State the blood parasite species.
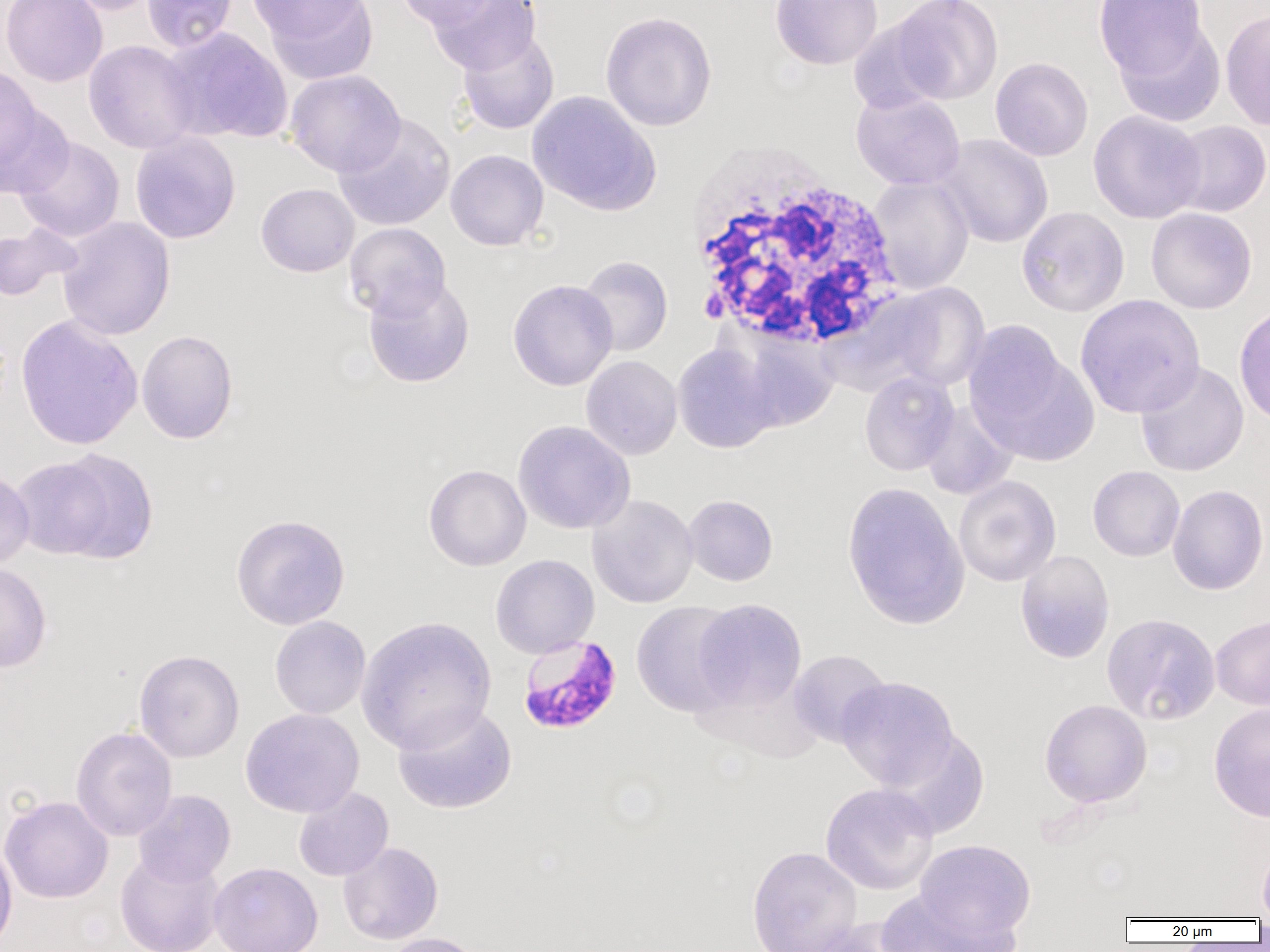

Plasmodium falciparum.

Approximate bounding boxes as [x1, y1, x2, y2] in pixels. White blood cell locations: [685, 141, 907, 355]. Uninfected red blood cell locations: [1, 0, 108, 87], [63, 0, 164, 15], [142, 0, 237, 52], [245, 0, 369, 44], [394, 0, 502, 29], [425, 0, 540, 74], [770, 0, 883, 70], [891, 0, 1004, 104], [1094, 0, 1209, 83], [258, 2, 378, 82], [147, 4, 256, 90], [1220, 7, 1270, 131], [600, 11, 718, 131], [847, 17, 949, 115], [1113, 18, 1226, 128], [163, 28, 293, 144], [457, 29, 559, 135], [83, 40, 200, 154], [990, 57, 1094, 161], [0, 66, 42, 174], [284, 69, 406, 177], [851, 90, 966, 191], [527, 91, 661, 216], [0, 98, 75, 199], [1087, 110, 1207, 224], [334, 114, 456, 231], [1168, 120, 1270, 217], [130, 131, 241, 244], [936, 134, 1054, 248], [16, 136, 125, 242], [445, 149, 549, 250], [868, 176, 974, 294], [256, 183, 360, 277], [1016, 206, 1130, 317], [1146, 208, 1258, 314], [57, 217, 175, 341], [344, 222, 451, 320], [0, 224, 79, 302], [577, 255, 673, 357], [363, 276, 475, 388], [507, 278, 618, 390], [883, 282, 991, 392], [1075, 294, 1205, 418], [1234, 302, 1270, 426], [15, 314, 143, 452], [964, 325, 1097, 465], [724, 328, 840, 433], [136, 329, 238, 444], [672, 342, 782, 454], [581, 355, 682, 460], [1135, 361, 1249, 477], [859, 371, 959, 476], [920, 401, 1018, 500], [513, 420, 635, 534], [43, 448, 159, 564], [423, 464, 531, 571], [1087, 466, 1185, 561], [0, 468, 35, 569], [954, 475, 1061, 586], [841, 482, 971, 631], [1167, 484, 1269, 595], [588, 494, 698, 608], [683, 494, 778, 586], [230, 513, 351, 630], [1015, 550, 1116, 663], [490, 554, 599, 658], [0, 562, 52, 672], [691, 599, 807, 712], [631, 601, 743, 717], [1101, 612, 1221, 725], [1210, 614, 1270, 711], [269, 616, 371, 720], [356, 616, 497, 754], [134, 649, 245, 763], [788, 649, 892, 748], [836, 676, 958, 791], [1039, 699, 1152, 808], [1209, 701, 1270, 823], [393, 703, 517, 814], [240, 707, 364, 817], [71, 726, 177, 841], [885, 728, 990, 839], [820, 783, 939, 895], [293, 787, 393, 881], [133, 789, 235, 887], [0, 795, 113, 904], [914, 839, 1036, 944], [0, 840, 18, 952], [1258, 840, 1270, 919], [338, 842, 443, 945], [746, 846, 863, 952], [115, 850, 225, 952], [208, 862, 323, 952], [875, 888, 1016, 952], [802, 920, 913, 952], [379, 932, 488, 952]. Plasmodium falciparum-infected red blood cell locations: [517, 634, 623, 736]. Image is 1270×952 pixels. Thin blood smear. 1000x magnification. Optical microscopy. Single field of view.